Name the parasite shown.
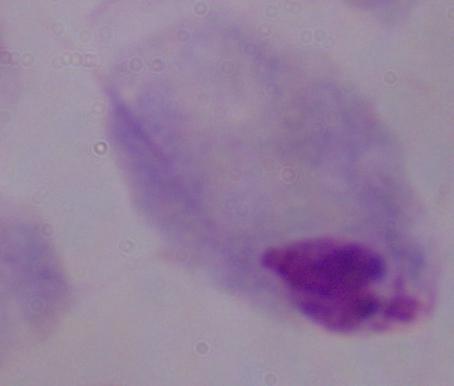

This is a trichomonad.

magnification = 1000x
modality = photomicrograph